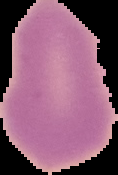

Summary:
  - Preparation: thin blood film
  - Result: negative for Plasmodium parasites
  - Image type: cell region segmented out of the field of view; surrounding area masked to black
  - Image size: 118×175 pixels